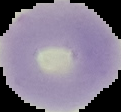
Summary:
  - Preparation: thin blood smear
  - Image size: 121×112 pixels
  - Image type: cell region segmented out of the field of view; surrounding area masked to black
  - Result: negative for malaria parasites